Name the parasite shown.
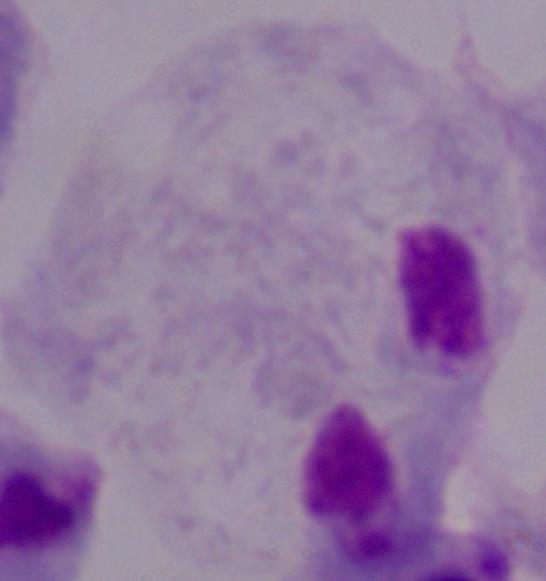
A trichomonad.

Summary:
  - Magnification: 1000x
  - Modality: micrograph